Report the malaria status of this cell.
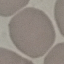
Uninfected.

Giemsa-stained preparation. Photographed with a smartphone camera at the microscope eyepiece. Thin blood film. Automatically extracted cell patch, resized to 64 × 64 pixels.